Assess this cell for malaria.
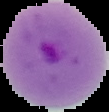

It is parasitized.

Image is 109×112 pixels. From a thin blood film. Segmented cell region on a black background.